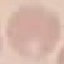
Summary:
  - Result: no malaria parasites seen
  - Preparation: thin smear
  - Capture: smartphone camera at the microscope eyepiece
  - Image type: cell patch, automatically extracted from a larger field of view and resized to 64 × 64 pixels
  - Stain: Giemsa